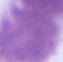

Summary:
  - Modality: micrograph
  - Identification: red blood cell
  - Magnification: 1000x